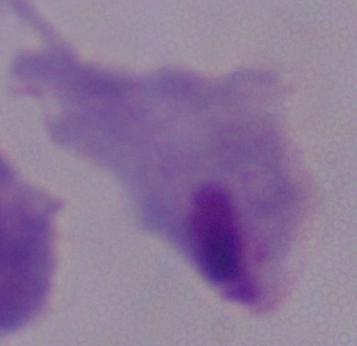
Summary:
  - Identification: trichomonad
  - Modality: photomicrograph
  - Magnification: 1000x